Assess this cell for malaria.
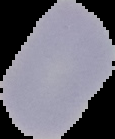
Uninfected.

image size = 115×139 pixels
image type = cell region segmented out of the field of view; surrounding area masked to black
preparation = thin blood film